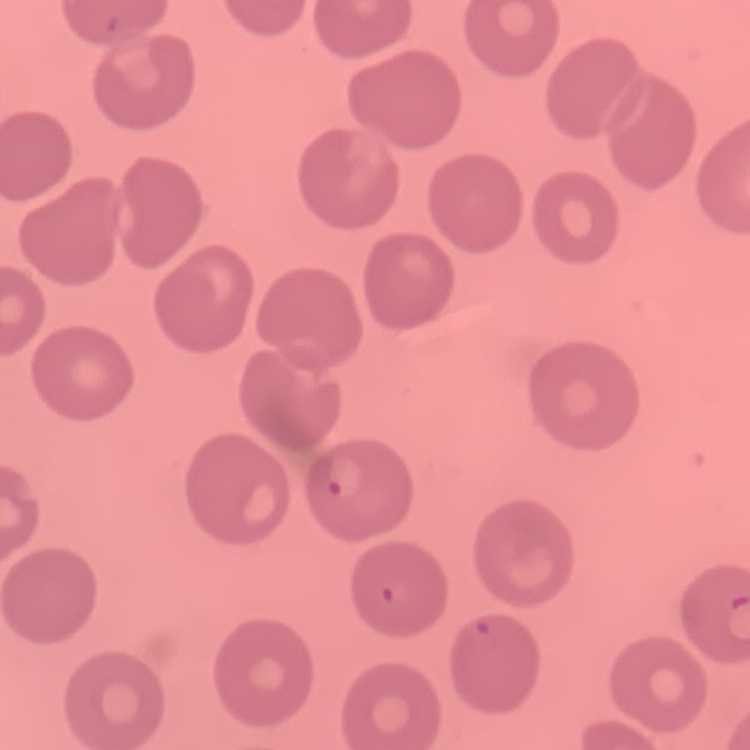

{
  "red_blood_cell_morphology": "no rouleaux formation",
  "image_type": "one tile cut from a larger photomicrograph",
  "stain": "Field's or Giemsa",
  "preparation": "thin peripheral smear"
}